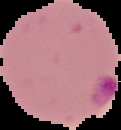
image type = segmented cell region on a black background
malaria status = parasitized
preparation = thin blood film
image size = 121×130 pixels